Give the extent of all Plasmodium falciparum-infected red blood cells.
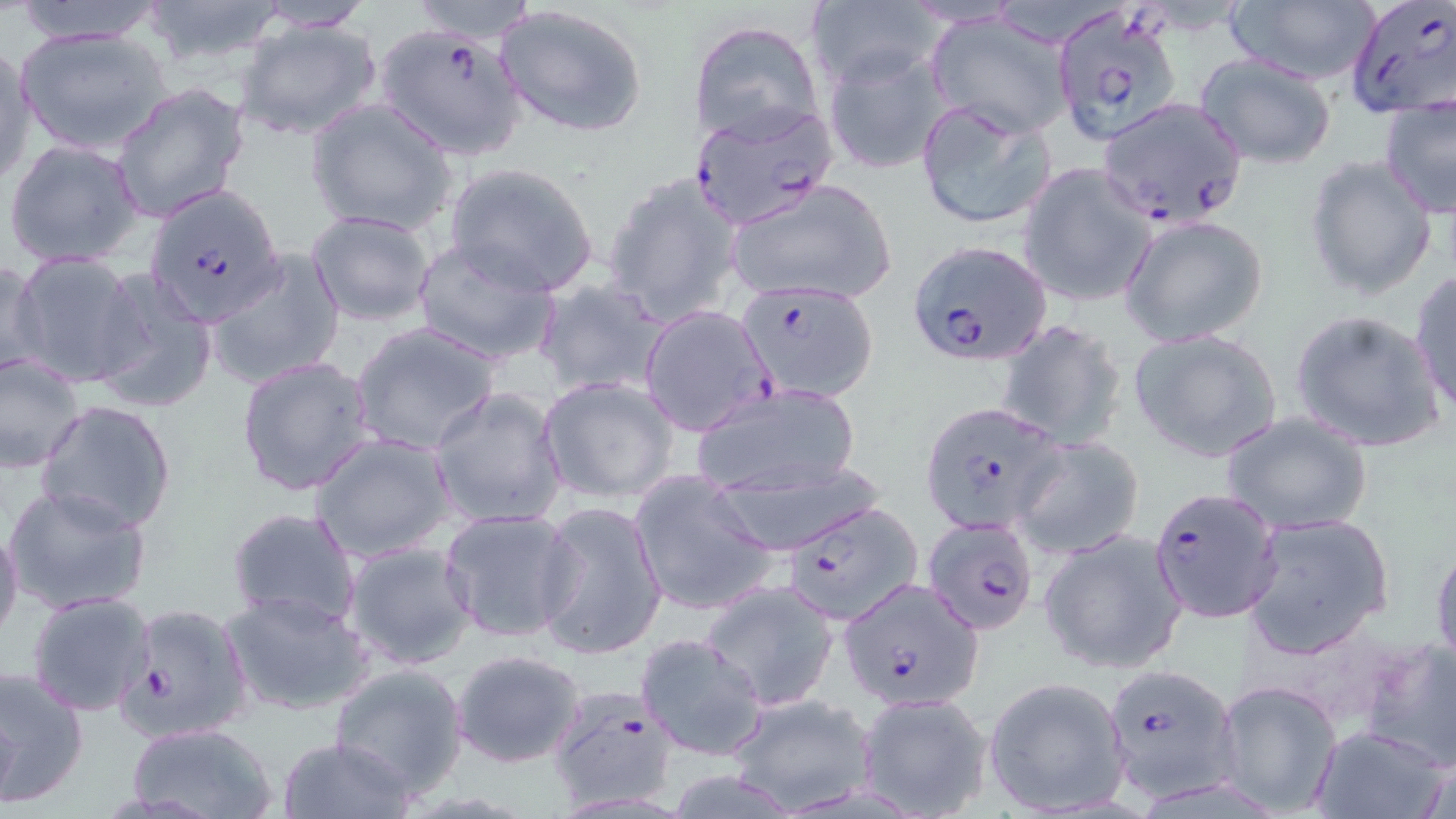
Approximate bounding boxes as [x1, y1, x2, y2] in pixels.
Plasmodium falciparum-infected red blood cells: [1348, 1, 1455, 120], [1050, 5, 1183, 144], [373, 22, 529, 162], [1098, 97, 1248, 228], [688, 104, 839, 230], [142, 183, 286, 324], [905, 240, 1050, 366], [735, 280, 881, 403], [639, 305, 775, 436], [920, 401, 1065, 536], [1150, 488, 1280, 619], [776, 503, 919, 628], [920, 516, 1040, 637], [839, 577, 984, 712], [116, 601, 255, 743], [1100, 661, 1243, 804], [543, 690, 677, 807].

Uninfected red blood cell locations: [9, 0, 170, 44], [136, 0, 293, 70], [402, 0, 544, 44], [1224, 0, 1382, 88], [245, 1, 376, 33], [809, 1, 940, 93], [494, 3, 650, 139], [926, 13, 1074, 138], [234, 18, 383, 143], [688, 19, 824, 146], [16, 24, 174, 156], [0, 42, 37, 190], [822, 47, 954, 176], [1192, 51, 1338, 169], [108, 82, 248, 223], [305, 97, 458, 237], [913, 97, 1058, 233], [1379, 97, 1456, 219], [4, 137, 146, 270], [1304, 153, 1439, 302], [443, 161, 600, 297], [1019, 162, 1159, 309], [601, 170, 744, 328], [725, 178, 896, 307], [305, 210, 438, 328], [1119, 214, 1269, 347], [411, 239, 561, 367], [10, 251, 145, 388], [206, 251, 344, 390], [1, 255, 48, 380], [87, 267, 219, 414], [1408, 271, 1456, 416], [534, 278, 667, 398], [1287, 308, 1447, 454], [993, 320, 1130, 450], [350, 322, 500, 456], [1128, 327, 1283, 462], [0, 351, 87, 471], [236, 355, 377, 497], [538, 375, 680, 503], [689, 383, 862, 499], [430, 387, 568, 530], [36, 399, 178, 535], [1221, 410, 1373, 535], [310, 432, 457, 563], [1011, 435, 1147, 560], [706, 460, 882, 556], [627, 471, 779, 617], [3, 484, 153, 616], [535, 499, 667, 663], [225, 506, 362, 631], [439, 507, 580, 643], [1240, 511, 1395, 660], [0, 523, 23, 646], [1429, 529, 1456, 672], [1037, 530, 1188, 675], [344, 540, 478, 670], [701, 582, 839, 711], [222, 588, 375, 717], [27, 591, 157, 716], [633, 632, 769, 762], [1358, 637, 1456, 775], [451, 648, 587, 768], [327, 662, 470, 797], [0, 665, 90, 808], [985, 676, 1131, 816], [1213, 681, 1342, 813], [725, 692, 879, 812], [856, 693, 993, 818], [123, 722, 280, 818], [1308, 723, 1451, 819], [276, 736, 417, 819]. Slide-level diagnosis: Plasmodium falciparum. 1000x magnification. May-Grünwald-Giemsa stain. Thin blood film. Optical microscopy. One field of a larger specimen. Image is 1456×819 pixels.